Locate every blood parasite and identify its species.
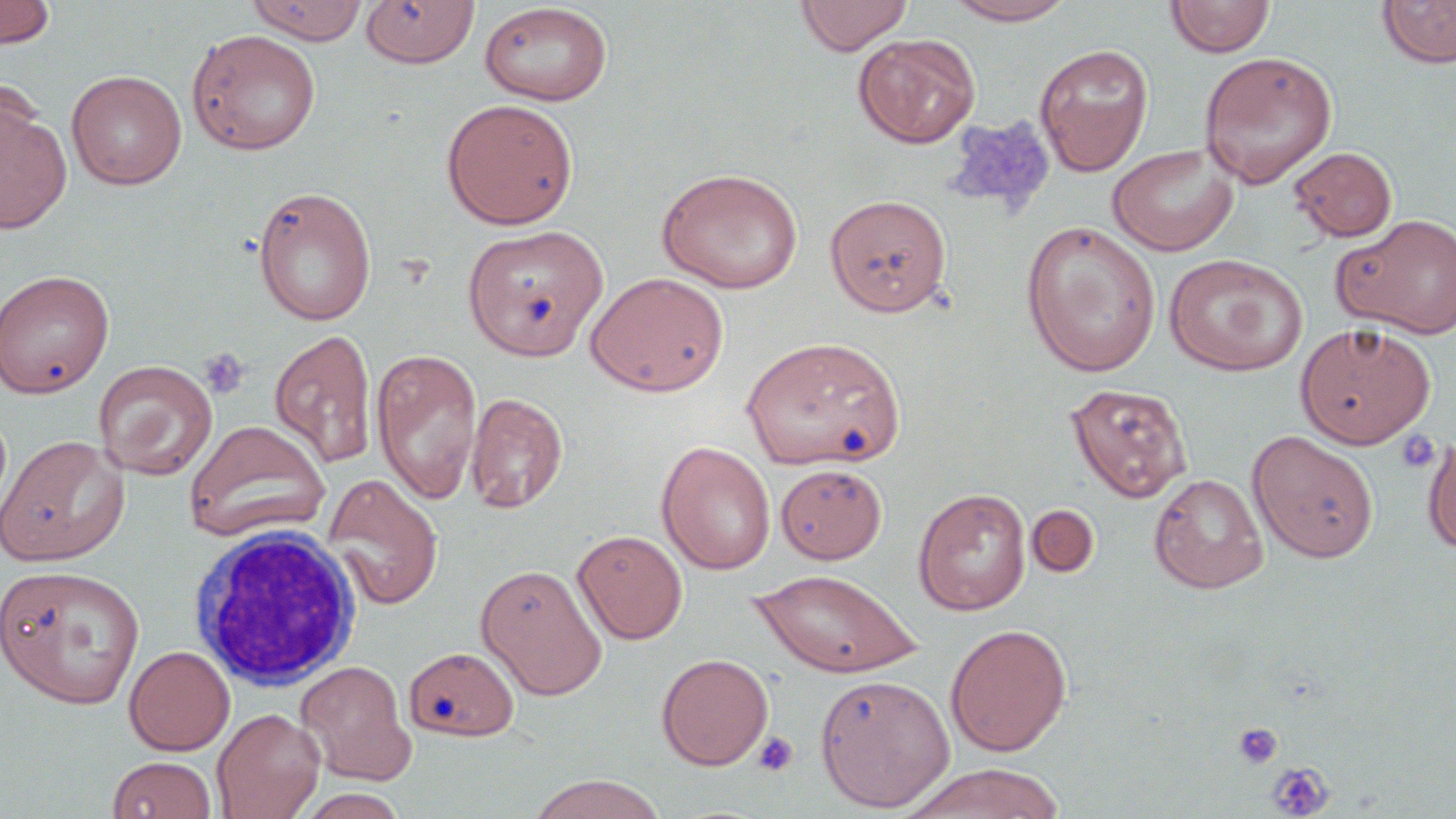
No blood parasites observed.

slide-level diagnosis = negative for blood parasites
uninfected red blood cell locations = approximate bounding boxes as (x1,y1)-(x2,y2) corner pairs in pixels: (0,0)-(56,49), (246,0)-(369,45), (794,0)-(913,56), (944,0)-(1078,25), (1165,0)-(1275,58), (1377,0)-(1456,69), (361,1)-(479,68), (479,3)-(613,106), (186,29)-(322,155), (853,33)-(981,148), (1035,44)-(1154,175), (1198,51)-(1338,188), (66,70)-(187,190), (441,98)-(578,229), (0,100)-(71,232), (1107,144)-(1238,257), (1289,147)-(1397,242), (657,167)-(802,293), (252,185)-(377,326), (825,194)-(953,316), (1333,213)-(1456,339), (1021,218)-(1161,376), (462,224)-(608,362), (1164,253)-(1308,377), (0,269)-(114,398), (584,271)-(730,397), (1295,322)-(1436,449), (269,328)-(377,469), (744,338)-(903,469), (371,348)-(483,506), (93,360)-(217,481), (1065,382)-(1193,503), (465,391)-(568,514), (183,419)-(331,542), (1246,430)-(1380,563), (1422,433)-(1456,554), (0,434)-(129,567), (656,440)-(776,574), (775,463)-(887,564), (322,473)-(443,611), (1149,473)-(1269,594), (913,487)-(1031,616), (1026,505)-(1099,578), (572,530)-(688,644), (475,563)-(609,700), (0,565)-(147,709), (751,568)-(922,678), (944,623)-(1072,756), (124,645)-(235,755), (403,646)-(522,741), (657,653)-(774,770), (295,660)-(416,785), (815,673)-(955,812), (212,708)-(325,819), (107,756)-(218,819), (900,763)-(1066,819), (525,773)-(669,819), (295,789)-(411,818)
field of view = one of a larger specimen
magnification = 1000x
image size = 1456×819 pixels
preparation = thin blood smear
modality = light microscopy
stain = May-Grünwald-Giemsa
platelet locations = approximate bounding boxes as (x1,y1)-(x2,y2) corner pairs in pixels: (944,116)-(1054,216), (198,347)-(249,400), (1396,428)-(1440,474), (1232,722)-(1284,770), (752,731)-(799,777), (1267,761)-(1335,818)
white blood cell locations = approximate bounding boxes as (x1,y1)-(x2,y2) corner pairs in pixels: (189,522)-(365,689)